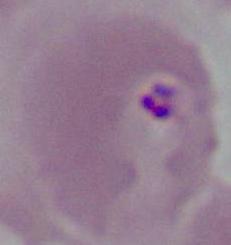

A Plasmodium parasite is seen. Micrograph. Captured at either 400x or 1000x magnification.